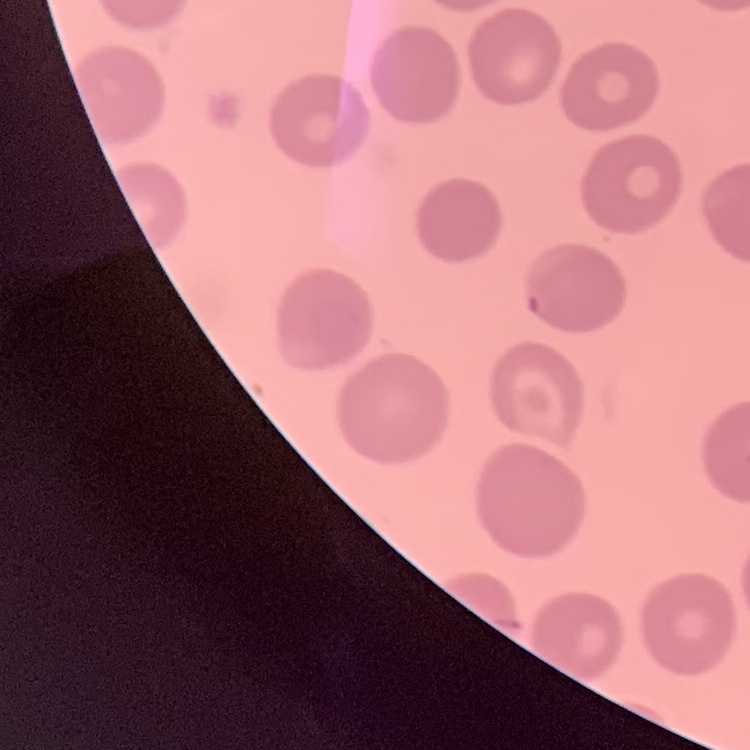

Summary:
  - Erythrocyte morphology: no rouleaux formation
  - Preparation: thin blood smear
  - Image type: one tile cut from a larger photomicrograph
  - Stain: Field's or Giemsa